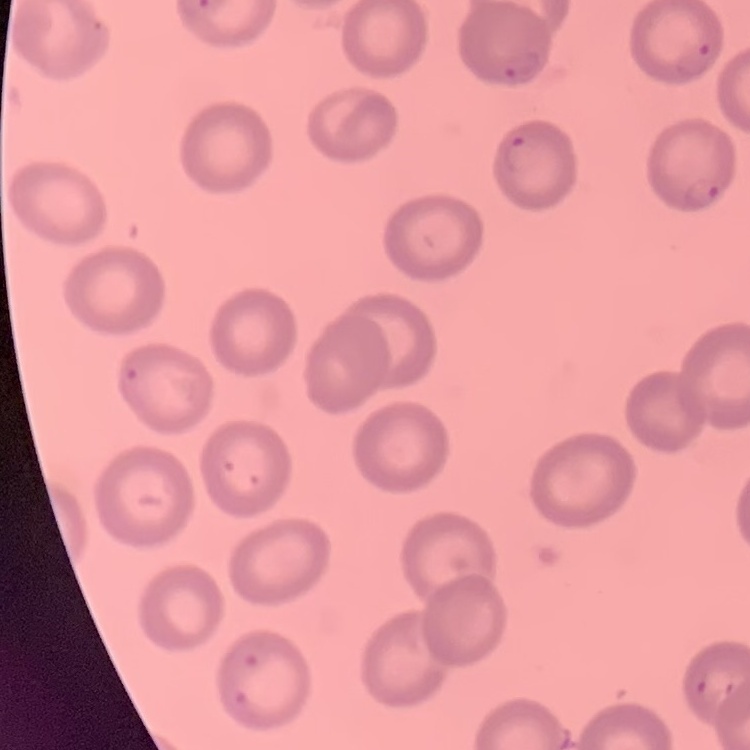
The red blood cells show no rouleaux formation. Thin blood film. Stained with either Field's or Giemsa. Square crop of a larger photomicrograph.